Comment on the morphology of the erythrocytes.
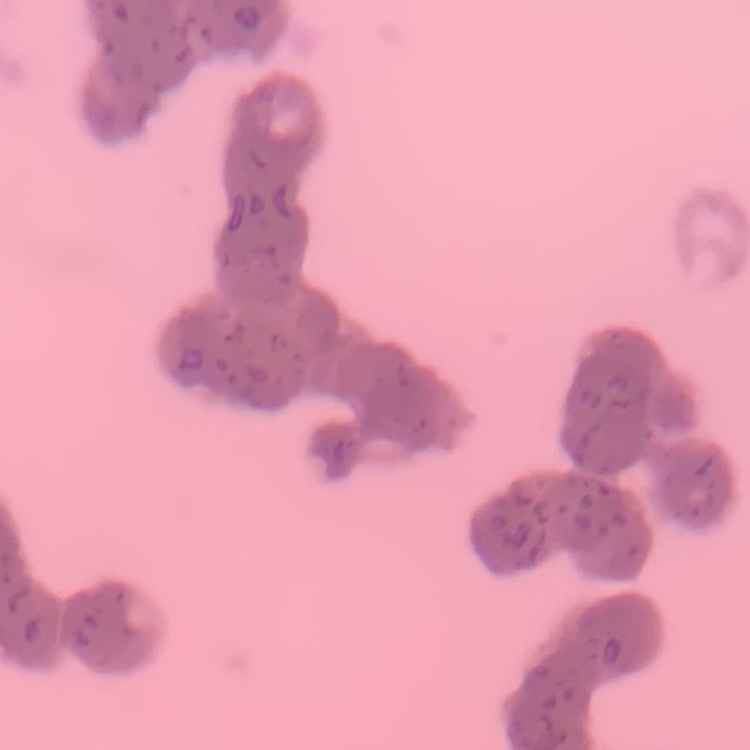
Rouleaux formation.

preparation = thin blood smear
image type = square crop of a larger photomicrograph
stain = Field's or Giemsa